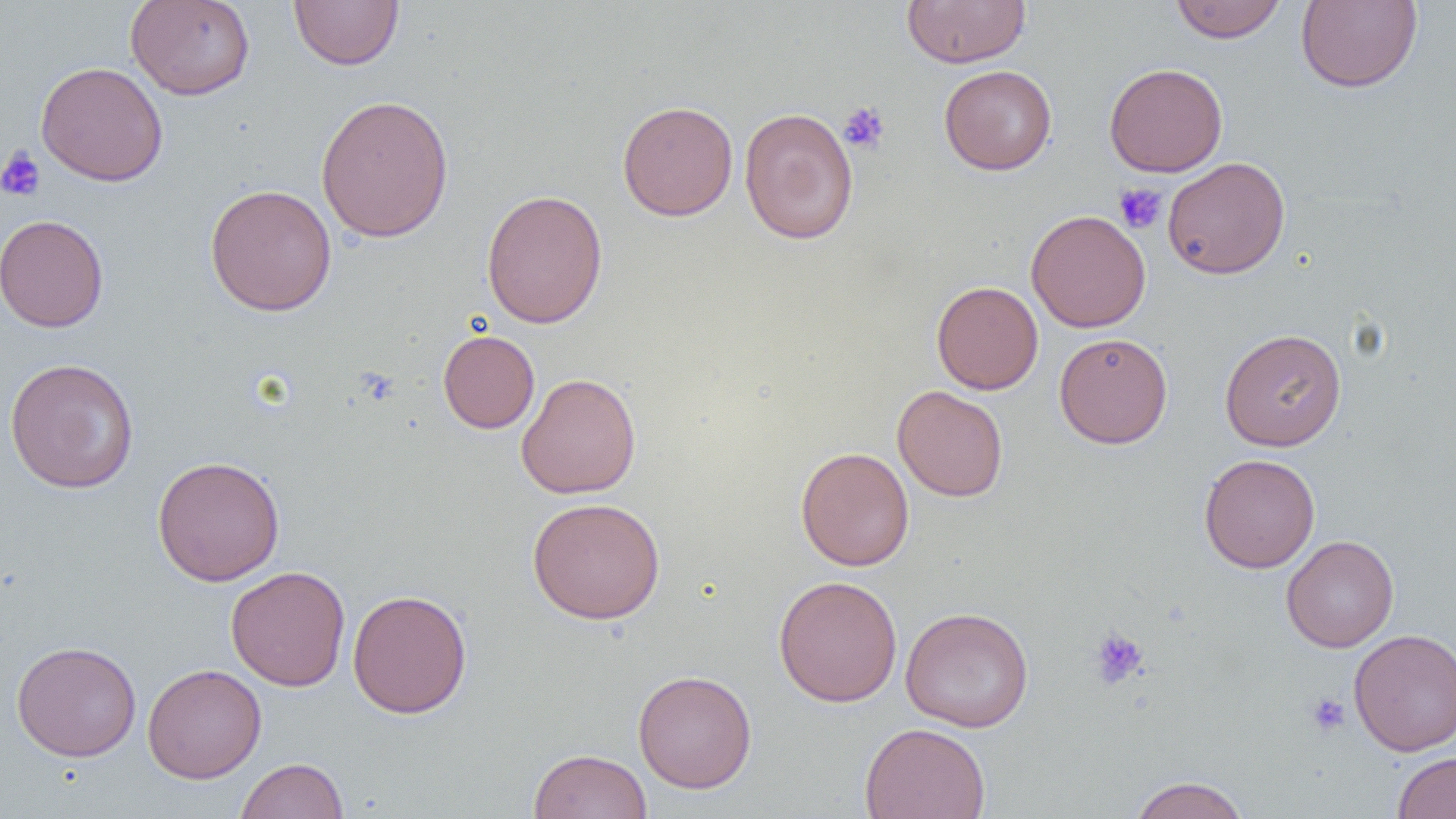 Approximate bounding boxes as named x1/y1/x2/y2 corners in pixels. Platelet locations: (x1=838, y1=102, x2=890, y2=154), (x1=0, y1=146, x2=46, y2=201), (x1=1113, y1=183, x2=1167, y2=234), (x1=1087, y1=626, x2=1149, y2=691), (x1=1305, y1=692, x2=1351, y2=738). Uninfected red blood cell locations: (x1=125, y1=0, x2=256, y2=100), (x1=289, y1=0, x2=404, y2=71), (x1=901, y1=0, x2=1030, y2=68), (x1=1169, y1=0, x2=1286, y2=43), (x1=1296, y1=0, x2=1423, y2=93), (x1=35, y1=61, x2=168, y2=186), (x1=1104, y1=62, x2=1228, y2=177), (x1=939, y1=65, x2=1057, y2=175), (x1=316, y1=93, x2=454, y2=244), (x1=617, y1=100, x2=738, y2=221), (x1=739, y1=107, x2=858, y2=245), (x1=1162, y1=157, x2=1290, y2=279), (x1=205, y1=184, x2=337, y2=316), (x1=481, y1=188, x2=608, y2=328), (x1=1026, y1=210, x2=1151, y2=333), (x1=0, y1=213, x2=109, y2=332), (x1=931, y1=281, x2=1043, y2=394), (x1=1219, y1=327, x2=1347, y2=451), (x1=437, y1=329, x2=540, y2=433), (x1=1054, y1=332, x2=1173, y2=449), (x1=3, y1=357, x2=140, y2=493), (x1=516, y1=373, x2=641, y2=499), (x1=893, y1=385, x2=1009, y2=502), (x1=795, y1=446, x2=915, y2=571), (x1=1198, y1=453, x2=1320, y2=573), (x1=152, y1=455, x2=285, y2=586), (x1=527, y1=497, x2=666, y2=624), (x1=1281, y1=534, x2=1399, y2=652), (x1=225, y1=565, x2=351, y2=691), (x1=773, y1=575, x2=903, y2=707), (x1=347, y1=589, x2=472, y2=718), (x1=900, y1=606, x2=1035, y2=731), (x1=1348, y1=627, x2=1456, y2=757), (x1=11, y1=641, x2=142, y2=761), (x1=142, y1=663, x2=266, y2=783), (x1=633, y1=669, x2=757, y2=794), (x1=859, y1=723, x2=991, y2=819), (x1=528, y1=748, x2=653, y2=819), (x1=1392, y1=751, x2=1456, y2=818), (x1=235, y1=757, x2=349, y2=819), (x1=1128, y1=775, x2=1250, y2=819). Slide-level diagnosis: no evidence of blood parasites. Optical microscopy. Image is 1456×819 pixels. Captured at 1000x magnification. Thin blood film. Single field of view.